Report the malaria status of this cell.
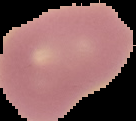

Uninfected.

Summary:
  - Image size: 136×121 pixels
  - Preparation: thin blood film
  - Image type: segmented cell region with the area outside set to black